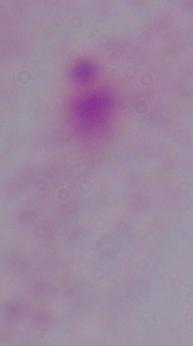

magnification = 1000x
modality = photomicrograph
identification = trichomonad